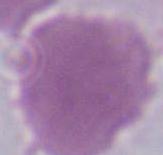 Photomicrograph. An erythrocyte is seen. 1000x magnification.